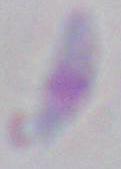

Summary:
  - Magnification: 1000x
  - Modality: photomicrograph
  - Identification: Toxoplasma gondii